Comment on the morphology of the erythrocytes.
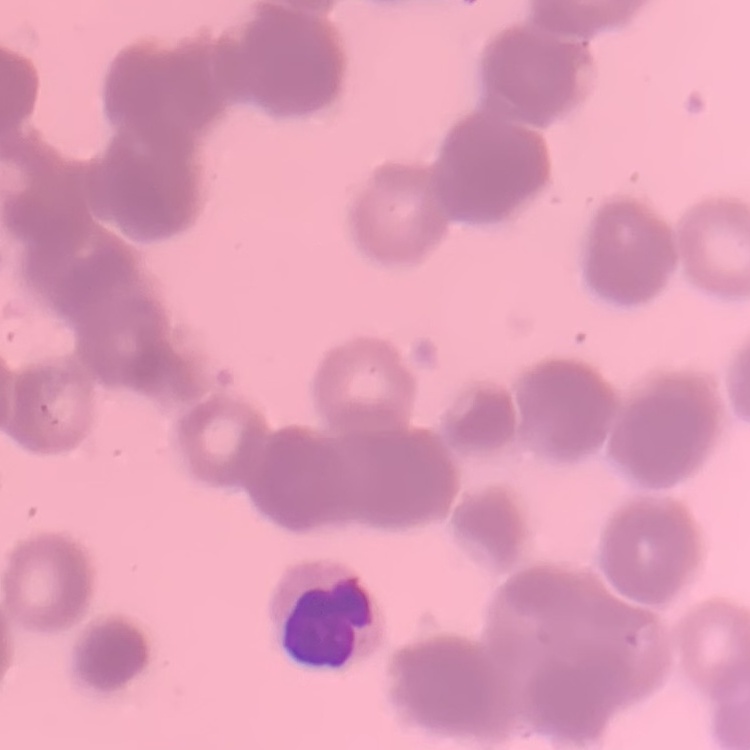

They show rouleaux formation.

Summary:
  - Stain: Field's or Giemsa
  - Preparation: thin blood smear
  - Image type: one tile cut from a larger photomicrograph